State which cell type is depicted.
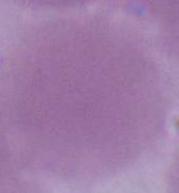
This is an erythrocyte.

Captured at 1000x magnification. Micrograph.